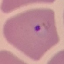

Summary:
  - Malaria status: parasitized
  - Image type: automatically extracted cell patch, resized to 64 × 64 pixels
  - Stain: Giemsa
  - Preparation: thin blood film
  - Capture: smartphone camera at the microscope eyepiece